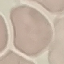

Summary:
  - Malaria status: uninfected
  - Image type: cell patch, automatically extracted from a larger field of view and resized to 64 × 64 pixels
  - Preparation: thin blood smear
  - Stain: Giemsa
  - Capture: smartphone through the microscope eyepiece